Give the extent of all uninfected red blood cells.
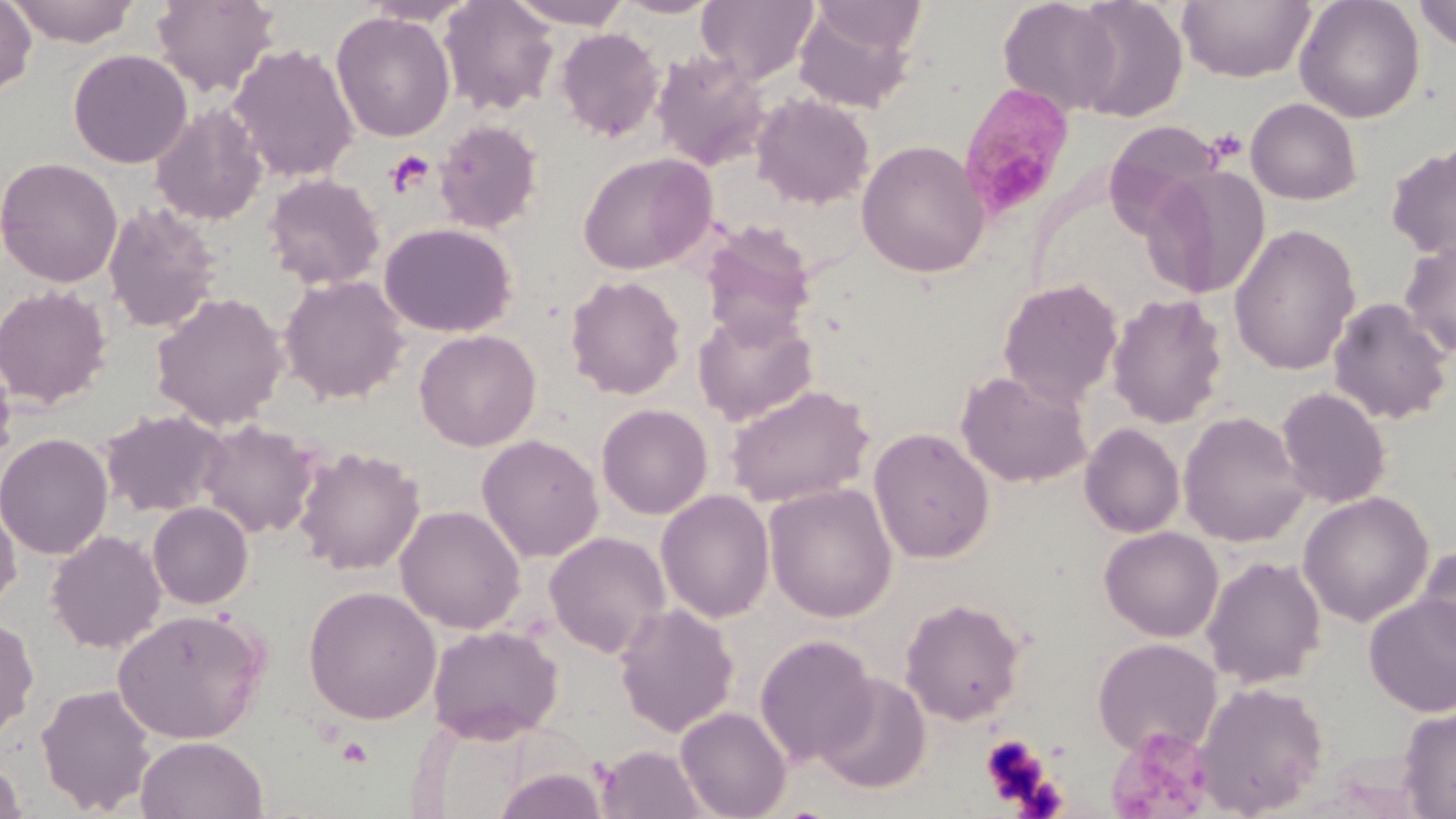

Approximate bounding boxes as (x1, y1, x2, y2) in pixels.
Uninfected red blood cells: (0, 0, 37, 98), (5, 0, 141, 47), (438, 0, 560, 116), (507, 0, 634, 29), (613, 0, 724, 19), (697, 0, 819, 85), (998, 0, 1121, 116), (1069, 0, 1189, 122), (1178, 0, 1316, 83), (1295, 0, 1425, 123), (1414, 0, 1456, 51), (151, 1, 280, 97), (359, 1, 481, 26), (793, 2, 921, 113), (331, 11, 456, 142), (555, 28, 665, 141), (228, 43, 360, 183), (68, 49, 192, 169), (651, 50, 772, 171), (750, 92, 875, 210), (1245, 97, 1362, 205), (149, 103, 268, 225), (433, 119, 545, 234), (1104, 121, 1226, 240), (856, 139, 989, 278), (1386, 144, 1456, 261), (577, 152, 717, 275), (0, 157, 123, 288), (1142, 164, 1269, 300), (262, 172, 386, 291), (103, 203, 222, 335), (698, 222, 816, 346), (379, 223, 518, 337), (1228, 223, 1362, 376), (1399, 237, 1456, 358), (278, 275, 410, 404), (565, 275, 686, 400), (997, 278, 1123, 407), (0, 285, 113, 409), (150, 292, 288, 430), (1107, 293, 1228, 428), (1327, 297, 1454, 425), (693, 307, 818, 426), (414, 329, 541, 451), (0, 347, 18, 471), (956, 369, 1092, 488), (726, 383, 875, 508), (1276, 387, 1391, 508), (596, 403, 713, 520), (99, 408, 229, 517), (1178, 411, 1309, 548), (195, 419, 323, 540), (1080, 423, 1185, 538), (868, 427, 995, 564), (0, 432, 114, 560), (477, 433, 604, 563), (293, 445, 425, 576), (764, 482, 898, 623), (656, 489, 775, 623), (1297, 490, 1434, 627), (0, 493, 21, 617), (147, 501, 254, 609), (395, 505, 526, 634), (1099, 526, 1223, 642), (46, 529, 167, 654), (544, 531, 672, 659), (1415, 544, 1456, 662), (1202, 556, 1326, 689), (303, 585, 441, 724), (1364, 594, 1456, 718), (900, 597, 1026, 726), (613, 602, 739, 737), (112, 608, 268, 744), (0, 614, 39, 741), (427, 624, 564, 744), (754, 634, 878, 767), (1092, 637, 1222, 756), (813, 673, 932, 795), (1193, 679, 1329, 816), (36, 682, 157, 815), (676, 706, 792, 819), (1397, 706, 1456, 818), (135, 734, 268, 819), (595, 745, 710, 819), (0, 755, 29, 819), (491, 766, 610, 819).

Platelet locations: (1205, 126, 1248, 166), (386, 150, 435, 196), (980, 733, 1053, 809), (337, 736, 372, 766). Plasmodium malariae-infected red blood cell locations: (957, 83, 1075, 220). Slide-level diagnosis: Plasmodium malariae. Optical microscopy. One field of a larger specimen. May-Grünwald-Giemsa-stained preparation. Thin blood film. Image is 1456×819 pixels. Captured at 1000x magnification.